Report the malaria status of this cell.
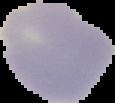

It is uninfected.

Segmented cell region on a black background. Image is 115×103 pixels. From a thin blood smear.